Assess this cell for malaria.
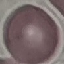

It is uninfected.

Summary:
  - Preparation: thin smear
  - Capture: smartphone camera at the microscope eyepiece
  - Stain: Giemsa
  - Image type: automatically extracted cell patch, resized to 64 × 64 pixels